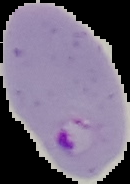
{
  "malaria_status": "parasitized",
  "image_type": "segmented cell region on a black background",
  "preparation": "thin blood film",
  "image_size": "130×184 pixels"
}